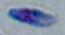
Summary:
  - Modality: photomicrograph
  - Magnification: 1000x
  - Identification: Toxoplasma gondii